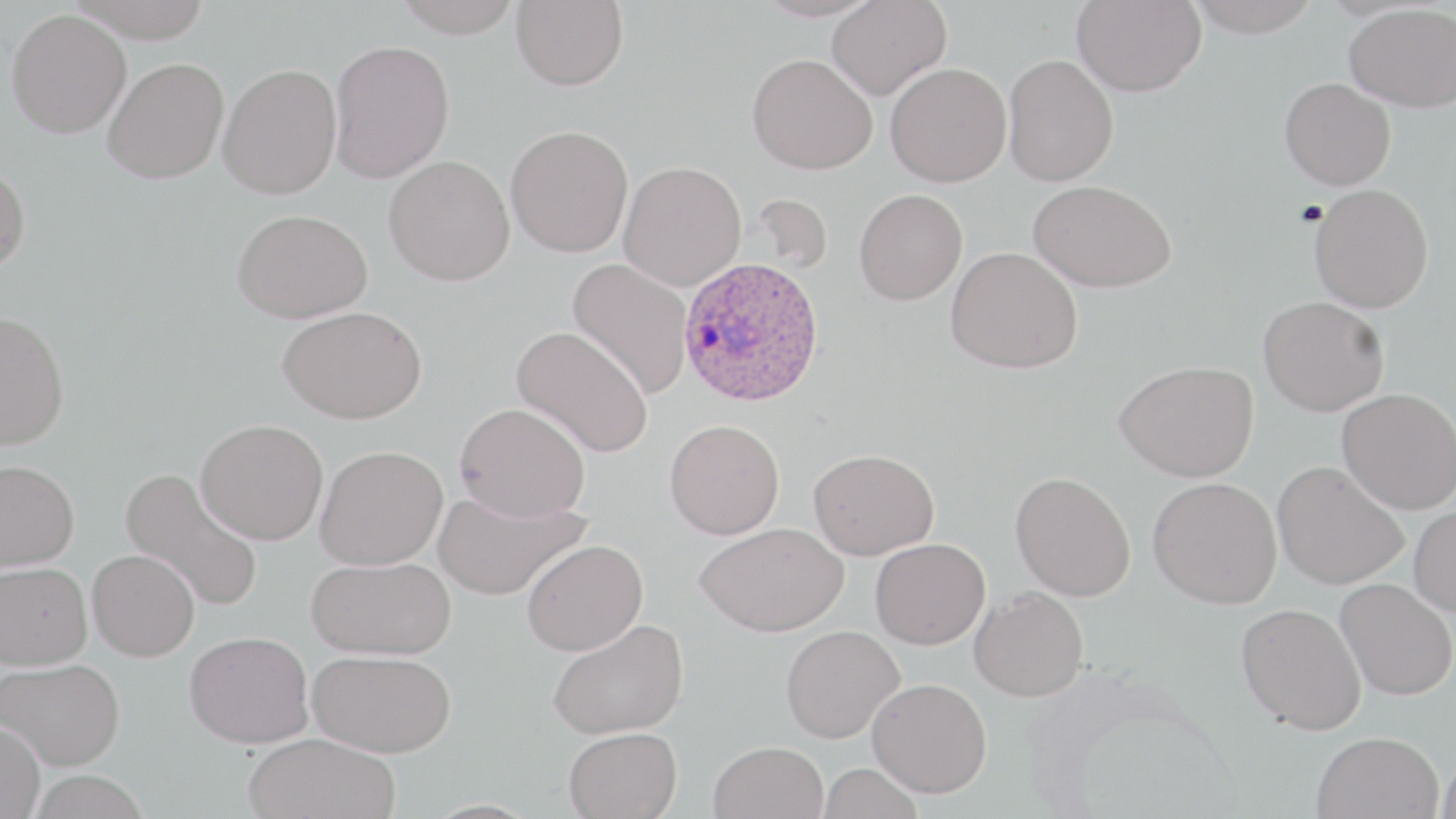
Approximate bounding boxes as [x1, y1, x2, y2] in pixels. Uninfected red blood cell locations: [67, 0, 214, 42], [391, 0, 525, 37], [511, 0, 629, 90], [827, 0, 951, 100], [1186, 0, 1322, 37], [1071, 1, 1207, 97], [1344, 3, 1456, 111], [5, 8, 132, 138], [328, 39, 455, 183], [747, 53, 878, 175], [1003, 53, 1119, 186], [103, 58, 229, 184], [885, 62, 1012, 187], [218, 63, 341, 199], [1280, 78, 1395, 190], [506, 124, 634, 258], [384, 155, 515, 286], [0, 160, 30, 277], [618, 161, 747, 291], [1028, 179, 1176, 292], [1309, 183, 1434, 313], [854, 189, 968, 305], [748, 193, 833, 277], [232, 208, 373, 323], [945, 246, 1083, 373], [567, 258, 694, 399], [1258, 296, 1389, 416], [278, 305, 427, 423], [0, 311, 70, 450], [511, 325, 653, 458], [1114, 359, 1259, 482], [1337, 388, 1456, 514], [455, 402, 590, 521], [196, 419, 328, 545], [664, 419, 784, 540], [315, 445, 448, 570], [809, 448, 939, 559], [0, 459, 79, 571], [1272, 461, 1408, 590], [120, 466, 264, 613], [1010, 471, 1136, 601], [1148, 476, 1282, 609], [434, 488, 588, 600], [1409, 504, 1456, 616], [695, 522, 848, 636], [870, 538, 990, 649], [522, 539, 648, 656], [87, 549, 200, 661], [306, 556, 456, 659], [0, 561, 92, 669], [1335, 578, 1456, 700], [970, 586, 1089, 701], [1236, 603, 1366, 734], [548, 618, 689, 739], [780, 626, 905, 743], [185, 631, 314, 748], [307, 649, 457, 757], [0, 658, 126, 770], [867, 678, 992, 797], [0, 721, 45, 819], [564, 727, 682, 819], [1312, 731, 1443, 819], [244, 732, 399, 819], [709, 741, 828, 819], [1436, 748, 1456, 818], [818, 763, 924, 819], [28, 771, 149, 819]. Plasmodium ovale-infected red blood cell locations: [677, 255, 826, 406]. Slide-level diagnosis: Plasmodium ovale. Light microscopy. Captured at 1000x magnification. One field of a larger specimen. Image is 1456×819 pixels. Thin blood film. May-Grünwald-Giemsa-stained preparation.